Assess the morphology of the erythrocytes.
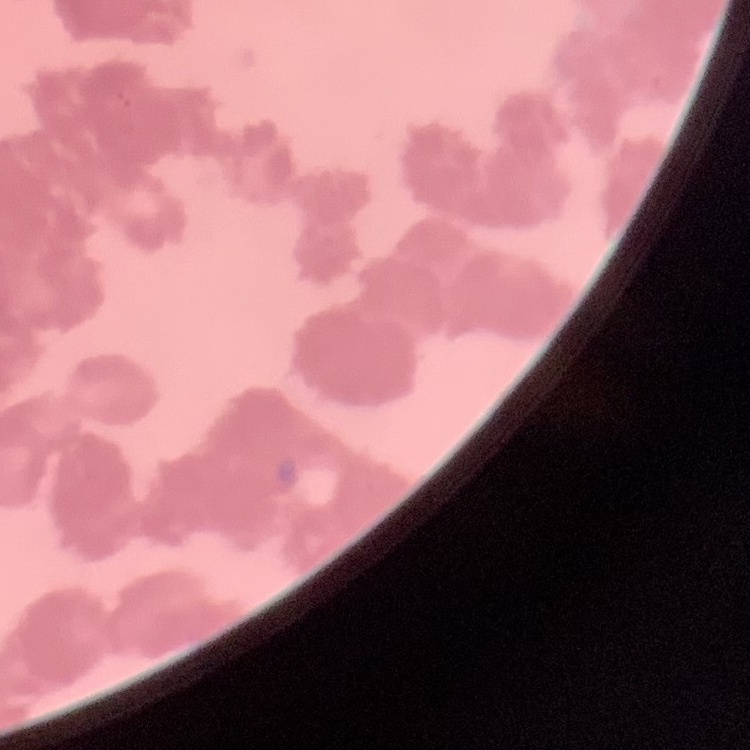
They show rouleaux formation.

image type = square crop of a larger photomicrograph
preparation = thin blood film
stain = Field's or Giemsa